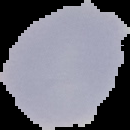

image size = 130×130 pixels
image type = segmented cell region with the area outside set to black
malaria status = uninfected
preparation = thin blood smear